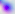
Captured at 400x magnification. Toxoplasma gondii is seen. Photomicrograph.